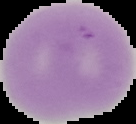
Summary:
  - Preparation: thin blood film
  - Result: negative for Plasmodium parasites
  - Image size: 136×124 pixels
  - Image type: segmented cell region on a black background